Identify the parasite.
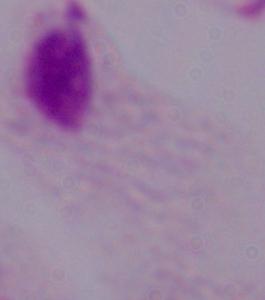
This is a trichomonad.

modality = micrograph
magnification = 1000x